Describe the morphology of the erythrocytes.
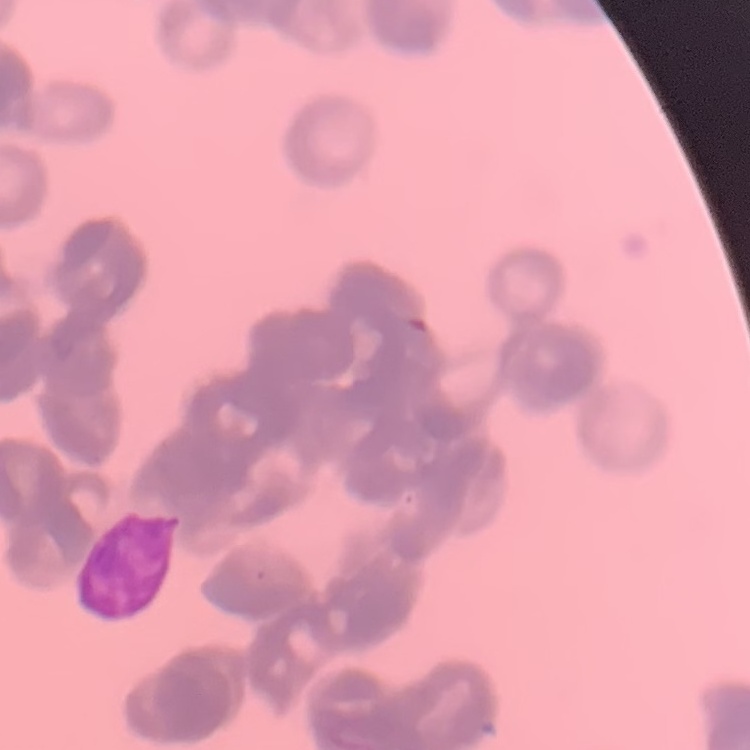

They show rouleaux formation.

stain = Field's or Giemsa
preparation = thin peripheral smear
image type = one tile cut from a larger photomicrograph